Identify the parasite.
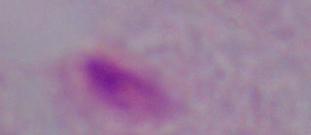
A trichomonad.

1000x magnification. Micrograph.